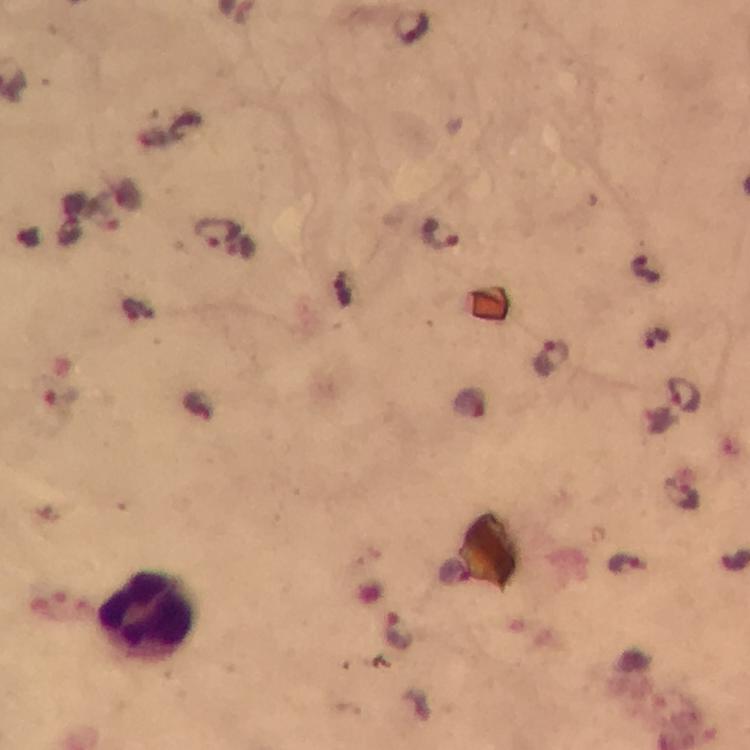

Approximate centers as (x, y) in pixels. Plasmodium parasite locations: (410, 25), (216, 231), (440, 234), (645, 267), (346, 290), (656, 338), (552, 358), (684, 395), (681, 495), (625, 565), (400, 630). Cropped region of a single field of view. From a diagnostic examination for malaria. 100x magnification. Giemsa stain. Image is 750×750 pixels. Immersion oil was used. Thick blood smear. Smartphone photograph taken through a microscope.